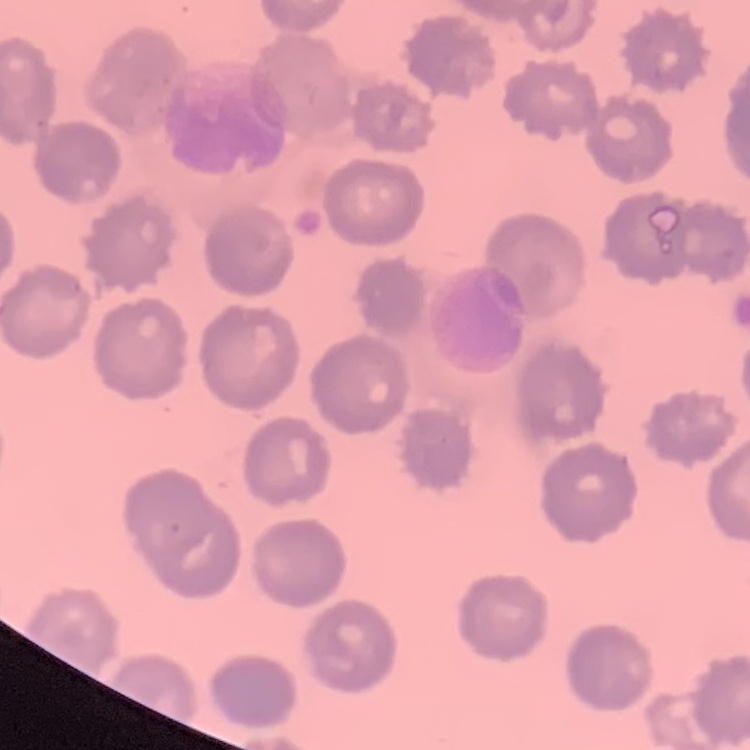

Summary:
  - Red blood cell morphology: no rouleaux formation
  - Stain: Field's or Giemsa
  - Image type: one tile cut from a larger photomicrograph
  - Preparation: thin peripheral smear